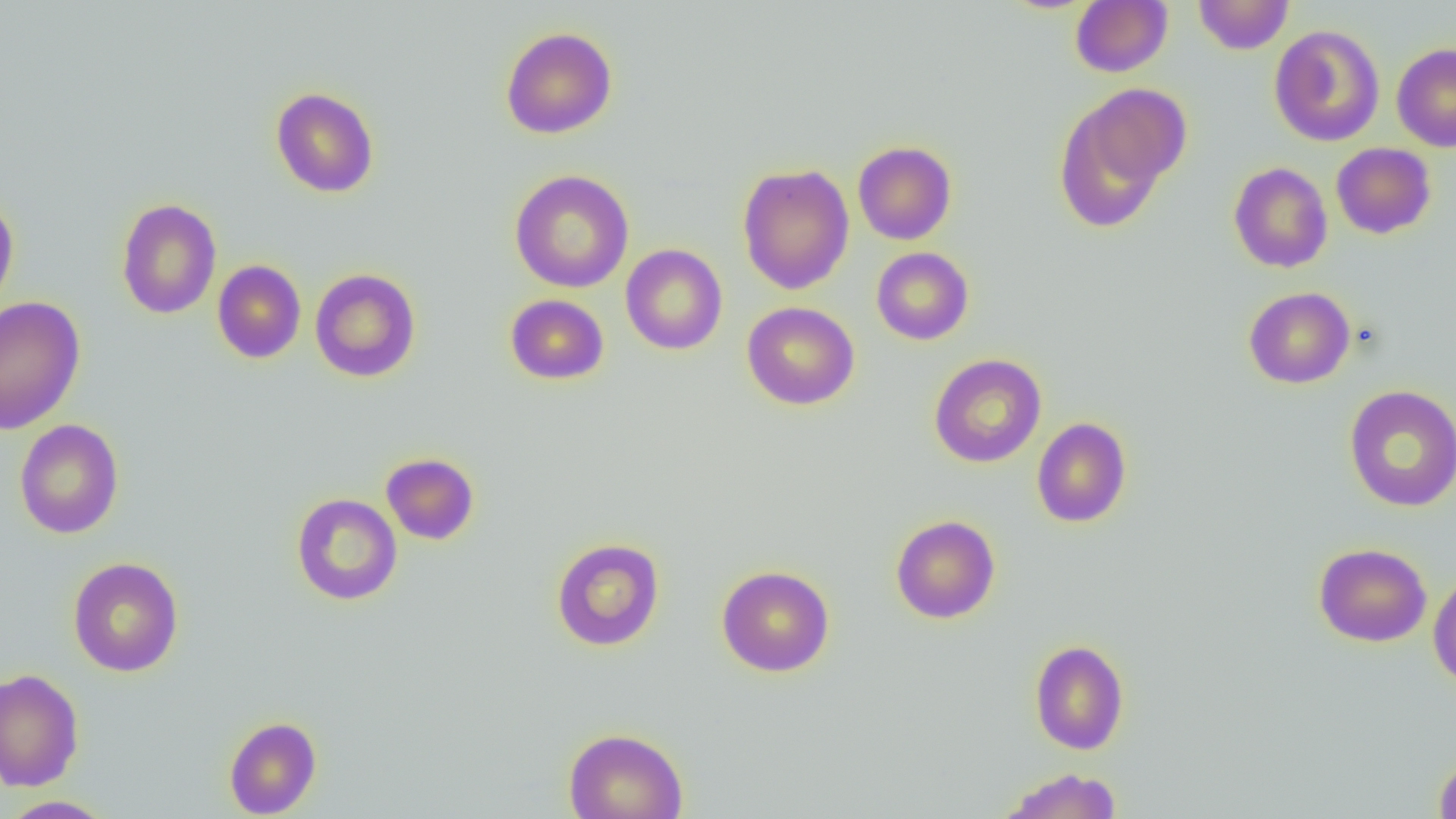

Summary:
  - Coordinate format: approximate bounding boxes as (x1,y1)-(x2,y2) corner pairs in pixels
  - Uninfected red blood cell locations: (1070,0)-(1172,77), (1193,0)-(1294,55), (1269,24)-(1385,147), (500,26)-(617,139), (1391,43)-(1456,152), (270,87)-(379,198), (1054,88)-(1187,232), (853,141)-(956,245), (1331,143)-(1436,239), (1228,162)-(1333,273), (737,163)-(854,295), (510,169)-(634,293), (0,193)-(19,316), (116,198)-(221,319), (620,244)-(727,356), (871,247)-(974,345), (212,259)-(306,364), (309,268)-(421,382), (1243,286)-(1355,389), (504,294)-(610,385), (0,296)-(86,435), (742,301)-(860,410), (928,353)-(1047,468), (1343,384)-(1455,512), (1031,417)-(1133,528), (14,419)-(124,539), (381,452)-(480,545), (291,492)-(403,606), (890,514)-(1001,624), (551,537)-(665,651), (1314,542)-(1432,647), (67,557)-(184,677), (716,565)-(835,677), (1428,569)-(1456,690), (1029,639)-(1130,755), (0,669)-(84,791), (224,716)-(322,818), (563,727)-(689,819), (1434,756)-(1456,818), (999,767)-(1123,819), (1,795)-(118,818)
  - Slide-level diagnosis: no evidence of blood parasites
  - Preparation: thin blood smear
  - Image size: 1456×819 pixels
  - Modality: optical microscopy
  - Field of view: single
  - Magnification: 1000x